Assess this cell for malaria.
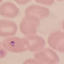
Uninfected.

Summary:
  - Capture: smartphone through the microscope eyepiece
  - Preparation: thin blood film
  - Image type: cell patch, automatically extracted from a larger field of view and resized to 64 × 64 pixels
  - Stain: Giemsa